Locate every blood parasite and identify its species.
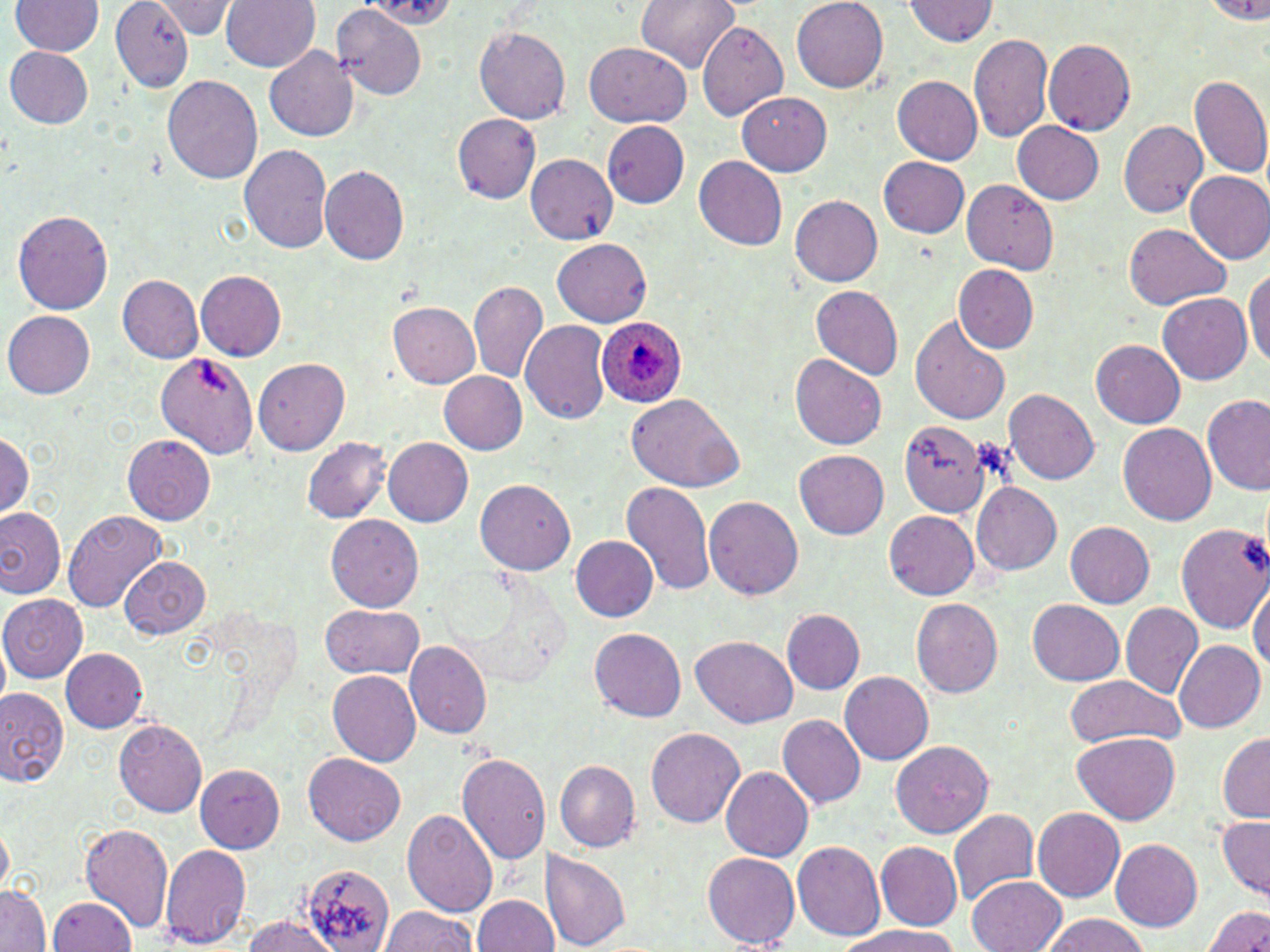
Approximate bounding boxes as (x1, y1, x2, y2) in pixels.
Plasmodium ovale-infected red blood cells: (596, 317, 689, 407).
No Plasmodium falciparum, Plasmodium malariae, Plasmodium vivax, Babesia divergens, or Trypanosoma brucei observed.

Uninfected red blood cell locations: (11, 0, 103, 56), (110, 0, 194, 94), (221, 0, 321, 72), (635, 0, 740, 72), (792, 0, 888, 92), (905, 0, 999, 45), (152, 1, 239, 38), (359, 1, 458, 26), (1202, 1, 1270, 24), (330, 6, 425, 98), (695, 21, 788, 120), (473, 26, 572, 124), (969, 32, 1053, 143), (1044, 38, 1136, 135), (585, 43, 691, 128), (4, 46, 94, 128), (264, 46, 358, 141), (1189, 75, 1270, 180), (163, 76, 262, 185), (893, 76, 984, 163), (738, 92, 831, 175), (452, 114, 541, 203), (1120, 120, 1208, 217), (602, 121, 690, 208), (1012, 122, 1103, 204), (239, 144, 333, 254), (525, 153, 618, 243), (693, 156, 786, 249), (879, 156, 970, 238), (319, 165, 410, 265), (1185, 170, 1270, 264), (962, 179, 1059, 275), (790, 195, 883, 287), (12, 210, 114, 315), (1123, 223, 1230, 310), (552, 237, 651, 326), (1244, 263, 1270, 369), (953, 265, 1038, 352), (196, 271, 286, 360), (118, 274, 204, 363), (469, 279, 548, 384), (812, 286, 903, 378), (1158, 293, 1252, 384), (389, 302, 481, 387), (3, 310, 95, 398), (911, 316, 1011, 425), (520, 320, 611, 425), (1092, 340, 1186, 428), (156, 349, 261, 457), (790, 353, 887, 451), (252, 358, 350, 456), (439, 370, 528, 453), (1004, 388, 1100, 485), (625, 393, 744, 492), (1203, 394, 1270, 497), (1118, 421, 1217, 525), (898, 423, 987, 516), (0, 433, 34, 518), (122, 435, 214, 524), (382, 436, 473, 526), (302, 438, 392, 523), (795, 450, 889, 538), (475, 478, 575, 575), (621, 480, 714, 598), (973, 482, 1061, 576), (704, 496, 803, 599), (0, 506, 65, 597), (63, 509, 167, 612), (883, 511, 979, 599), (326, 514, 423, 612), (1169, 518, 1269, 640), (1064, 521, 1155, 608), (1176, 522, 1268, 633), (571, 535, 658, 621), (120, 556, 210, 639), (1248, 579, 1269, 675), (1, 594, 86, 683), (911, 596, 1003, 698), (1029, 599, 1125, 686), (1121, 602, 1203, 697), (321, 603, 424, 679), (783, 609, 865, 694), (590, 629, 687, 721), (691, 635, 796, 728), (1173, 639, 1265, 733), (404, 641, 494, 738), (61, 647, 148, 732), (328, 669, 421, 767), (840, 671, 933, 766), (1065, 676, 1184, 747), (1, 689, 69, 788), (777, 714, 865, 809), (114, 719, 209, 817), (646, 727, 744, 827), (1073, 731, 1180, 825), (1217, 731, 1270, 821), (890, 740, 994, 837), (303, 753, 406, 846), (456, 753, 551, 865), (554, 760, 639, 851), (196, 762, 287, 851), (721, 766, 813, 862), (1032, 807, 1125, 902), (947, 808, 1041, 905), (402, 809, 498, 919), (1218, 813, 1270, 899), (0, 822, 14, 898), (81, 822, 174, 933), (1110, 839, 1202, 931), (791, 841, 885, 940), (876, 841, 962, 929), (159, 843, 250, 948), (541, 849, 634, 950), (703, 851, 800, 947), (301, 865, 395, 950), (966, 876, 1066, 952), (0, 885, 52, 951), (472, 893, 558, 951), (47, 896, 135, 951), (1201, 905, 1270, 952), (380, 906, 477, 952), (1039, 915, 1148, 952), (239, 916, 345, 952), (835, 925, 961, 952). Slide-level diagnosis: Plasmodium ovale. Light microscopy. Captured at 1000x magnification. Single field of view. May-Grünwald-Giemsa-stained preparation. Image is 1270×952 pixels. Thin blood film.